Look for Plasmodium parasites.
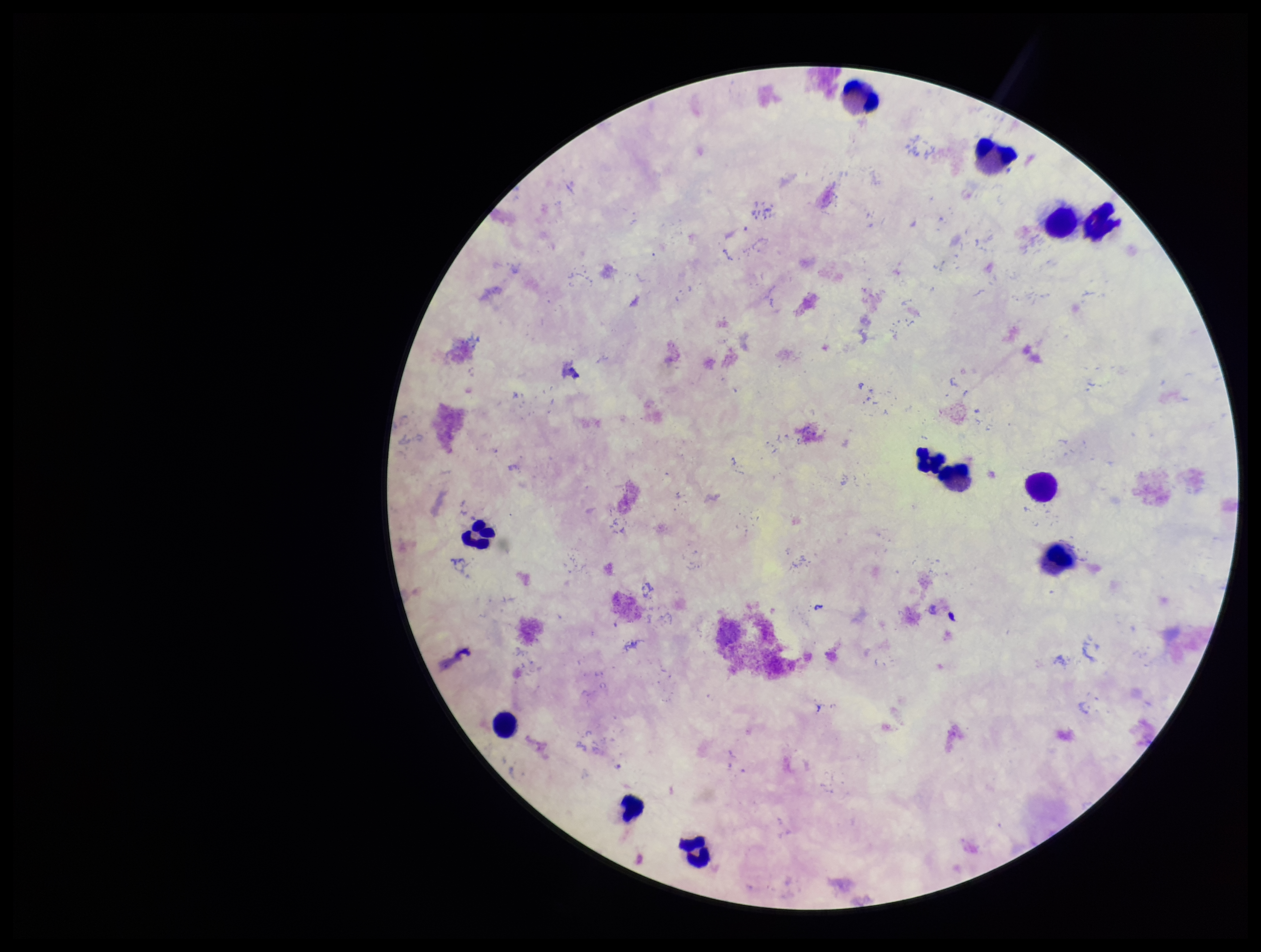

None identified.

Species reported for this patient: Plasmodium falciparum. Parasite count: 0. Preparation: thick blood smear. Leukocyte count: 11. Image is 1261×952 pixels. Stained with Giemsa. Patient malaria status: infected. Single field of view. Smartphone photograph taken through the eyepiece of a microscope.